Comment on the morphology of the red blood cells.
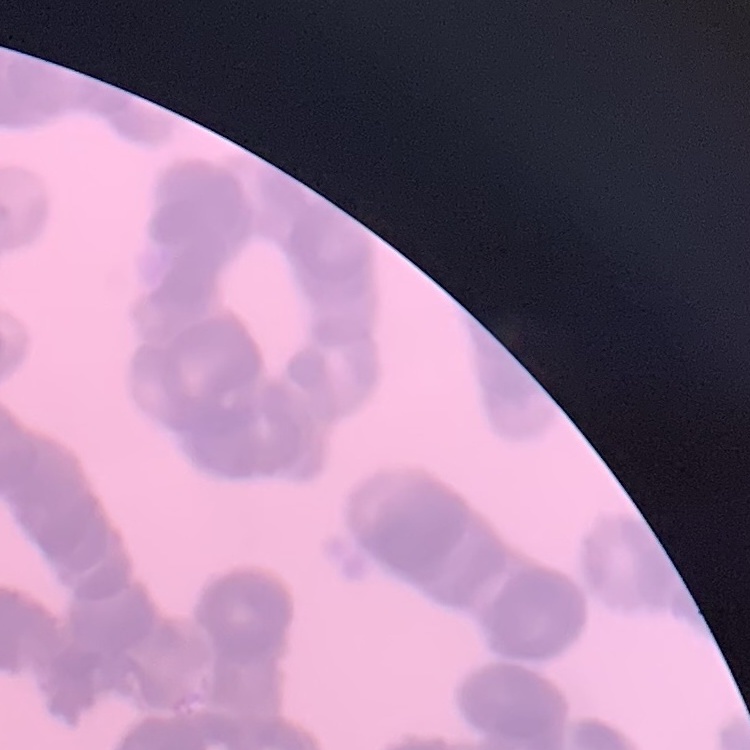

They show rouleaux formation.

Thin blood smear. Stained with either Field's or Giemsa. Square crop of a larger photomicrograph.